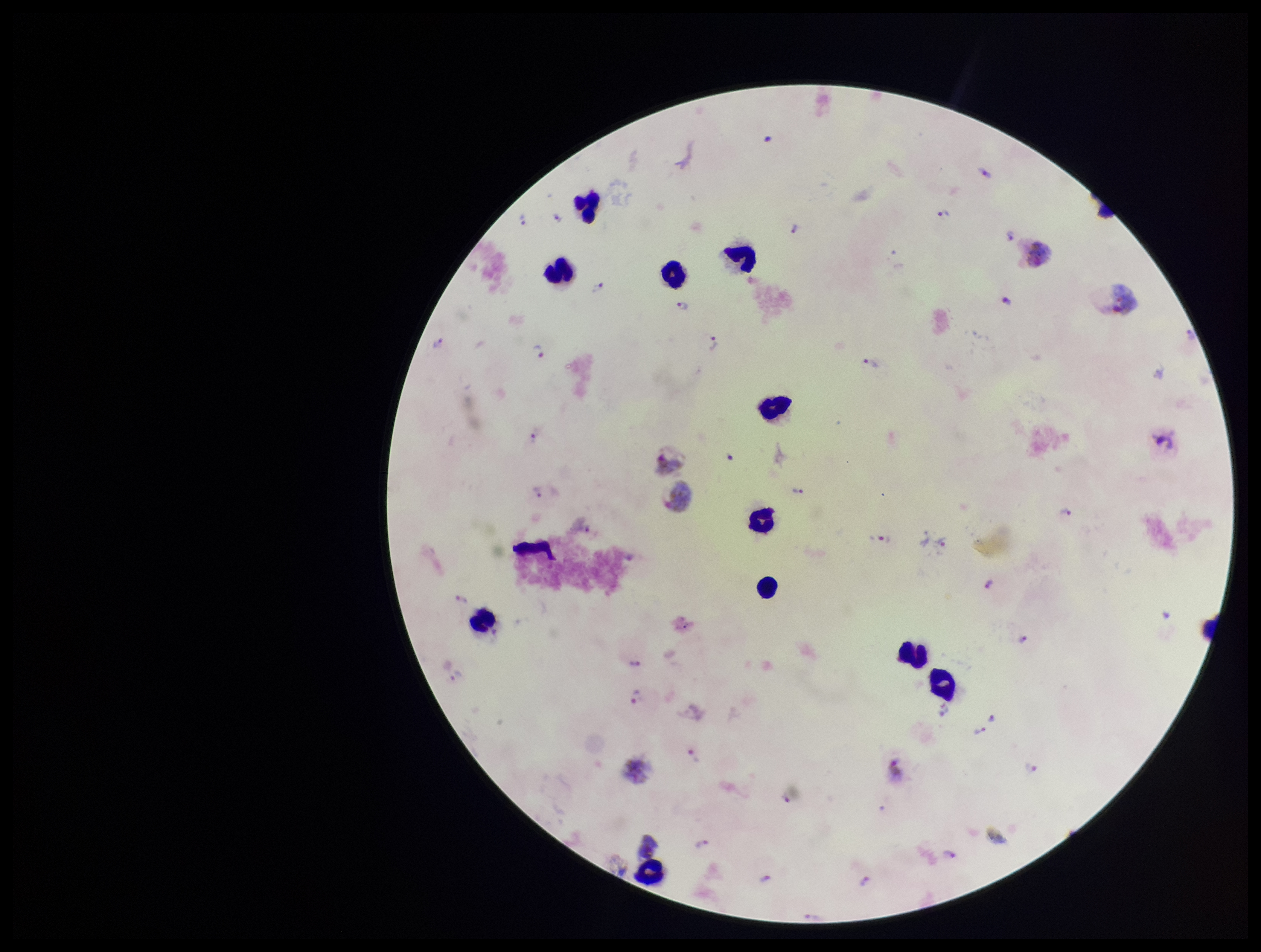
patient_malaria_status: infected
stain: Giemsa
leukocyte_count: 11
field_of_view: one from this slide
parasite_count: 30
plasmodium_parasites: detected
image_size: 1261×952 pixels
preparation: thick smear
species_reported_for_this_patient: Plasmodium vivax
capture: smartphone photograph through the microscope eyepiece